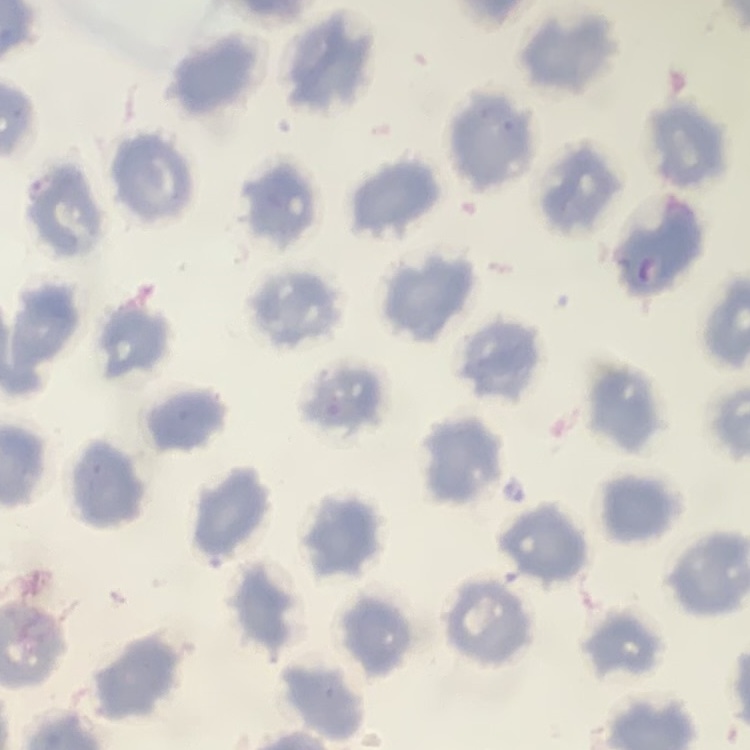

red blood cell morphology = no rouleaux formation
stain = Field's or Giemsa
preparation = thin blood film
image type = square crop of a larger photomicrograph